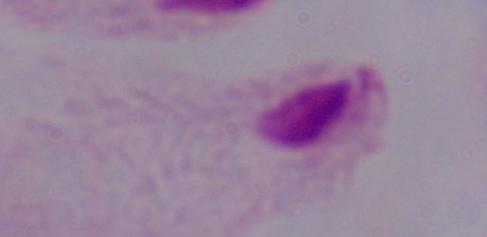
Summary:
  - Modality: micrograph
  - Identification: trichomonad
  - Magnification: 1000x